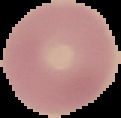
preparation = thin blood smear
malaria status = uninfected
image size = 121×118 pixels
image type = segmented cell region with the area outside set to black